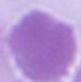 A red blood cell is shown. 1000x magnification. Photomicrograph.